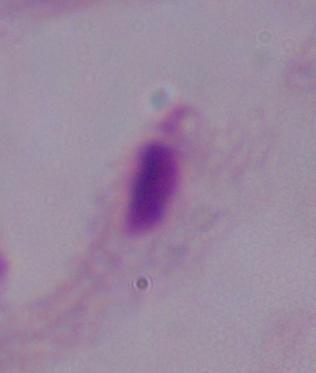

modality = photomicrograph
identification = trichomonad
magnification = 1000x